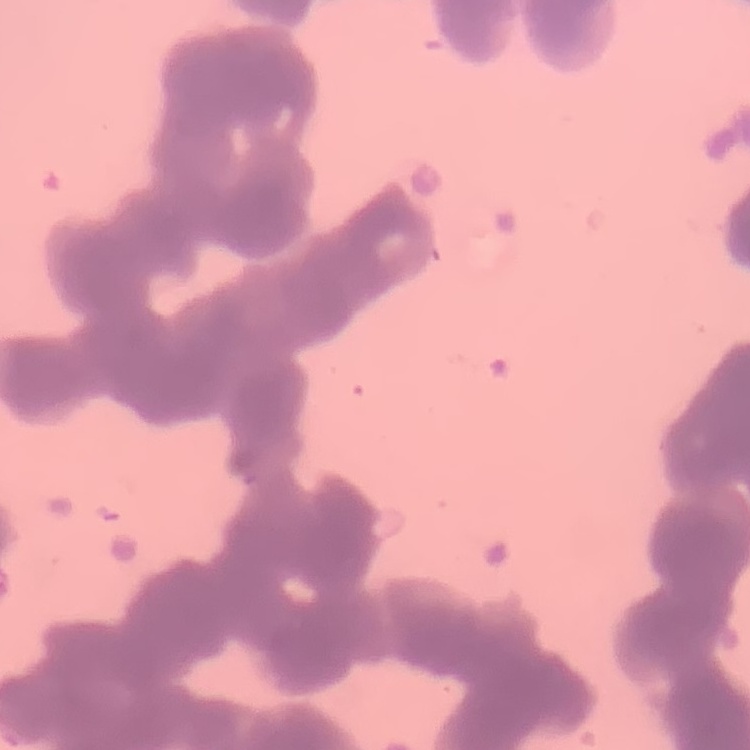

Summary:
  - Erythrocyte morphology: rouleaux formation
  - Image type: square crop of a larger photomicrograph
  - Stain: Field's or Giemsa
  - Preparation: thin blood film